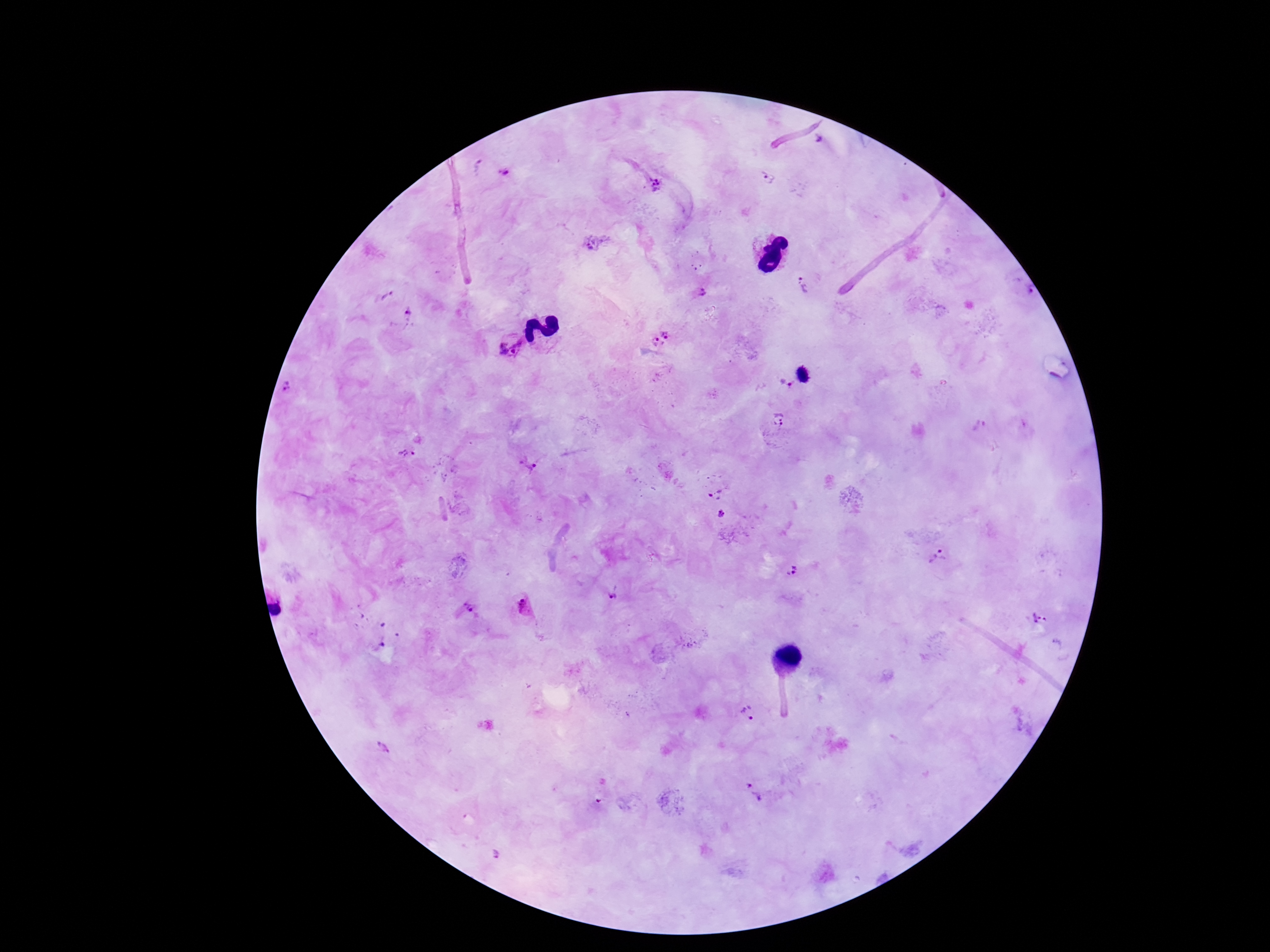

{
  "preparation": "thick blood film",
  "field_of_view": "one from this slide",
  "plasmodium_parasite_locations": "approximate object centers, in pixels from the top-left corner: (x=820, y=143), (x=479, y=166), (x=504, y=173), (x=766, y=180), (x=655, y=185), (x=596, y=241), (x=803, y=285), (x=1025, y=291), (x=699, y=292), (x=386, y=295), (x=408, y=313), (x=666, y=331), (x=654, y=343), (x=512, y=345), (x=787, y=384), (x=290, y=387), (x=779, y=419), (x=406, y=454), (x=527, y=465), (x=715, y=492), (x=721, y=515), (x=938, y=557), (x=790, y=570), (x=613, y=595), (x=282, y=604), (x=468, y=606), (x=524, y=607), (x=1040, y=618), (x=379, y=644), (x=748, y=713), (x=380, y=747), (x=752, y=792), (x=495, y=855)",
  "capture": "smartphone camera through the microscope eyepiece",
  "patient_malaria_status": "infected",
  "stain": "Giemsa",
  "image_size": "1270×952 pixels",
  "magnification": "100x"
}